Name the parasite shown.
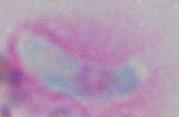
Toxoplasma gondii.

Micrograph. Captured at 1000x magnification.